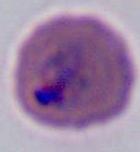
Summary:
  - Magnification: 400x or 1000x
  - Identification: Plasmodium
  - Modality: photomicrograph